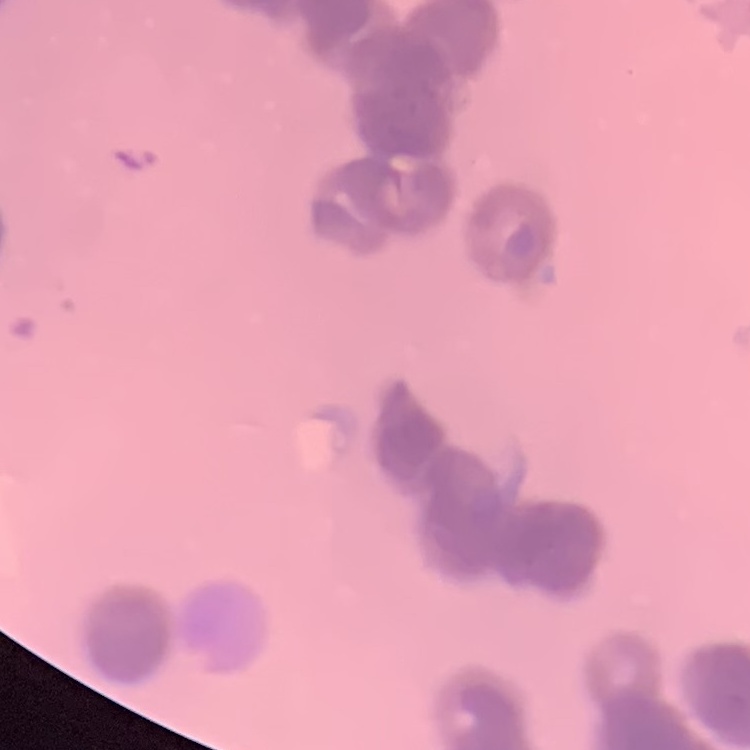

The erythrocytes exhibit rouleaux formation. One tile cut from a larger photomicrograph. Thin peripheral smear. Field's or Giemsa stain.